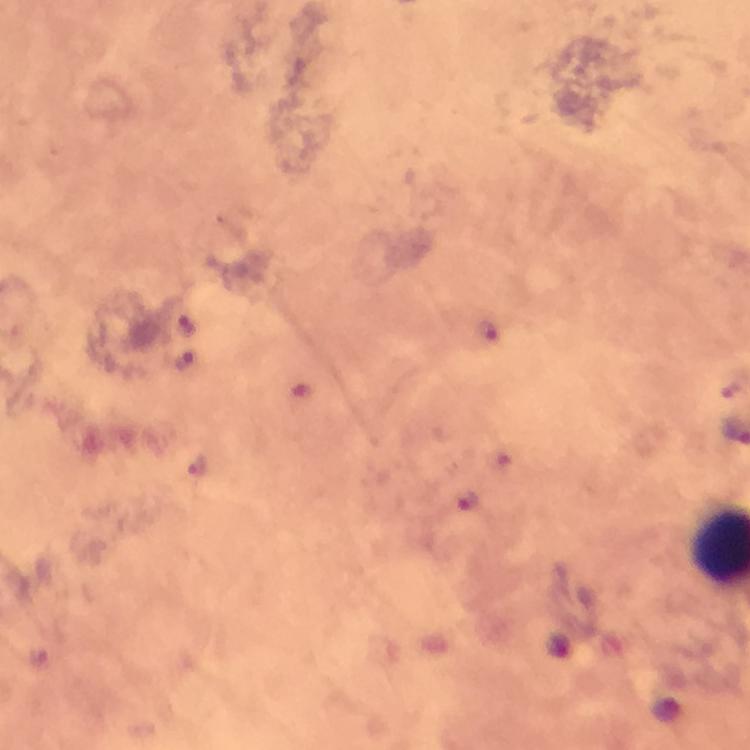 Approximate centers as [x, y] in pixels. Malaria parasite locations: [186, 327], [489, 333], [184, 359], [198, 465], [468, 502]. Thick blood smear. From a diagnostic examination for malaria. A crop from one field of view. Giemsa stain. Immersion oil applied. Photographed through the microscope with a smartphone camera. Image is 750×750 pixels. At 100x magnification.